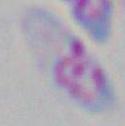 Captured at 1000x magnification. Toxoplasma gondii is seen. Photomicrograph.